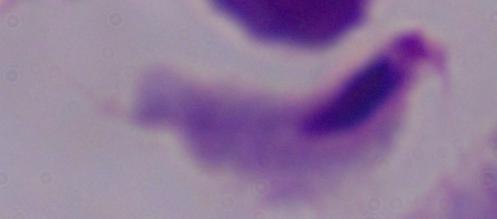
Captured at 1000x magnification. A trichomonad is seen. Micrograph.